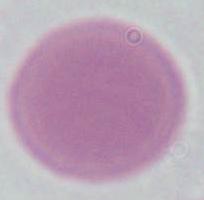

Summary:
  - Identification: red blood cell
  - Magnification: 1000x
  - Modality: micrograph